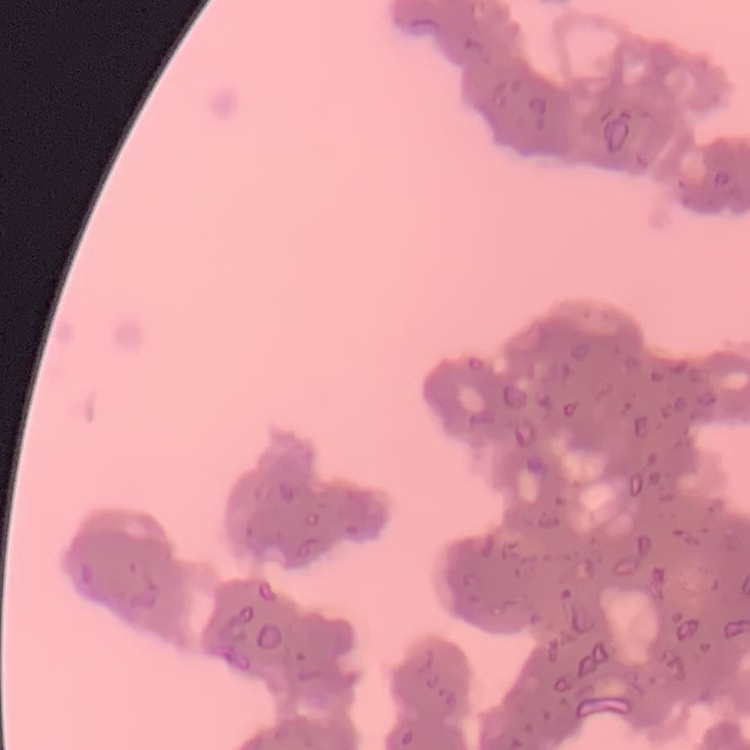

Summary:
  - Red blood cell morphology: rouleaux formation
  - Stain: Field's or Giemsa
  - Image type: square crop of a larger photomicrograph
  - Preparation: thin blood smear